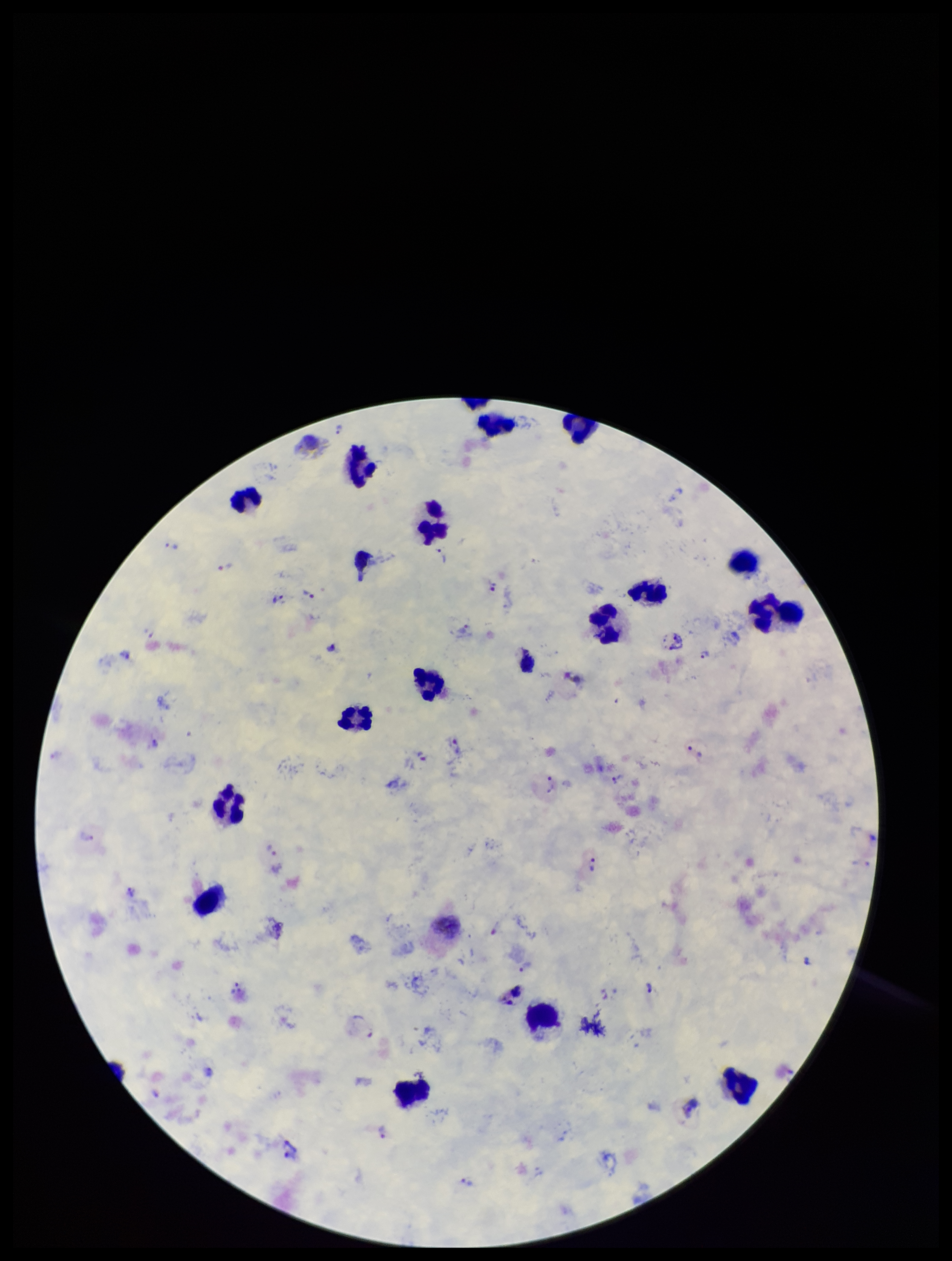

Preparation: thick blood smear. Plasmodium parasites: seen. Species reported for this patient: Plasmodium vivax. Photographed through the microscope eyepiece with a smartphone camera. Leukocyte count: 18. Patient malaria status: positive. Giemsa stain. Image is 952×1261 pixels. One field from this slide. Parasite count: 22.